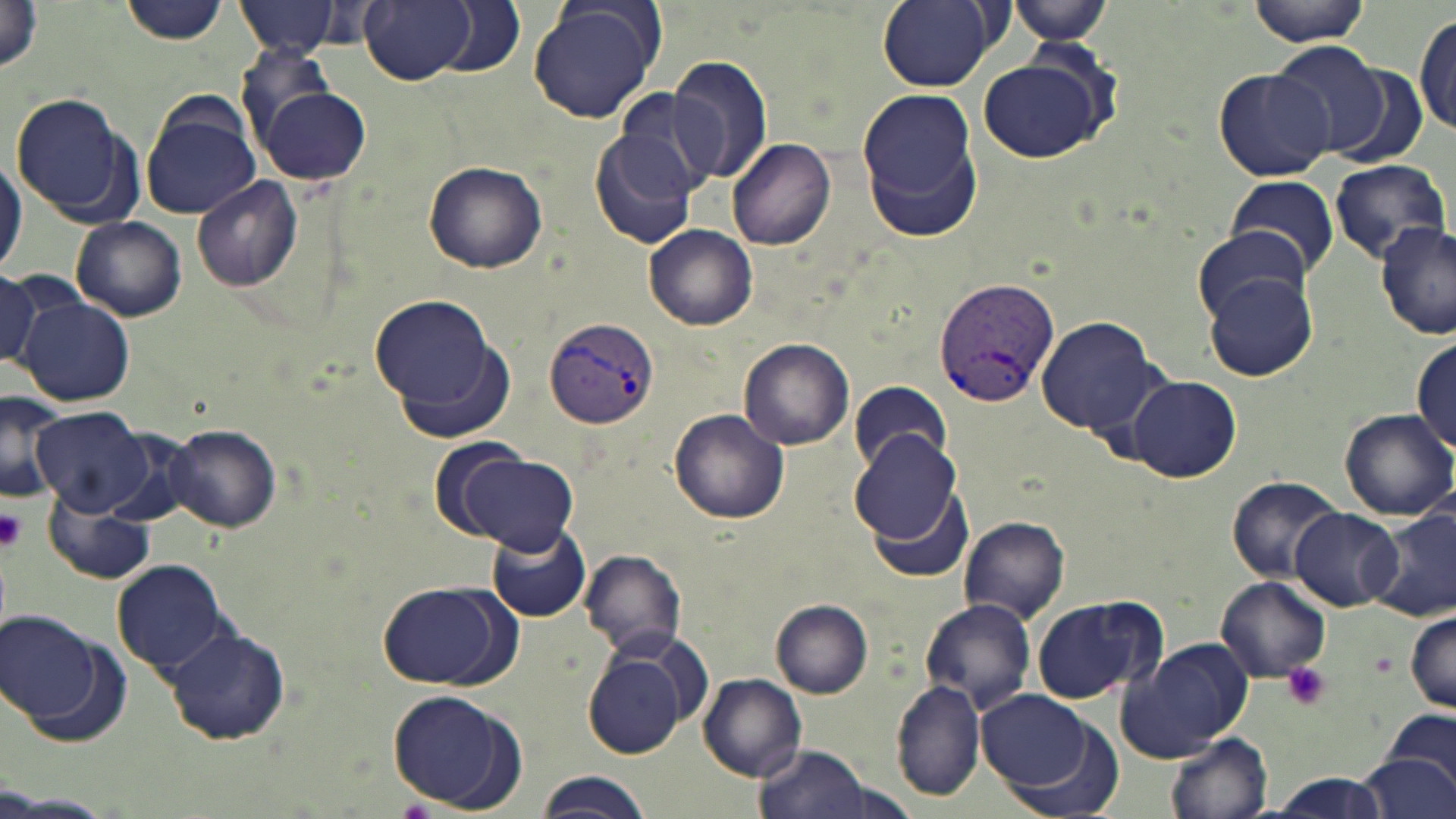
slide-level diagnosis = Plasmodium vivax
image size = 1456×819 pixels
modality = light microscopy
platelet locations = approximate bounding boxes as named x1/y1/x2/y2 corners in pixels: (x1=0, y1=507, x2=26, y2=552), (x1=1281, y1=663, x2=1331, y2=710)
magnification = 1000x
Plasmodium vivax-infected red blood cell locations = approximate bounding boxes as named x1/y1/x2/y2 corners in pixels: (x1=935, y1=280, x2=1058, y2=408), (x1=546, y1=317, x2=659, y2=428)
stain = May-Grünwald-Giemsa
uninfected red blood cell locations = approximate bounding boxes as named x1/y1/x2/y2 corners in pixels: (x1=1, y1=0, x2=44, y2=77), (x1=116, y1=0, x2=231, y2=44), (x1=235, y1=0, x2=348, y2=58), (x1=360, y1=0, x2=477, y2=85), (x1=877, y1=0, x2=998, y2=90), (x1=1008, y1=0, x2=1115, y2=46), (x1=1246, y1=0, x2=1374, y2=47), (x1=434, y1=1, x2=524, y2=77), (x1=528, y1=1, x2=664, y2=124), (x1=1414, y1=10, x2=1455, y2=141), (x1=1269, y1=42, x2=1393, y2=157), (x1=667, y1=55, x2=774, y2=188), (x1=977, y1=55, x2=1110, y2=162), (x1=1213, y1=67, x2=1335, y2=181), (x1=254, y1=81, x2=370, y2=186), (x1=857, y1=85, x2=979, y2=223), (x1=610, y1=90, x2=721, y2=199), (x1=7, y1=92, x2=141, y2=223), (x1=138, y1=99, x2=260, y2=219), (x1=169, y1=121, x2=293, y2=270), (x1=589, y1=124, x2=702, y2=250), (x1=728, y1=138, x2=836, y2=250), (x1=0, y1=150, x2=25, y2=279), (x1=1327, y1=158, x2=1450, y2=263), (x1=423, y1=159, x2=547, y2=272), (x1=1226, y1=175, x2=1341, y2=280), (x1=191, y1=177, x2=303, y2=292), (x1=72, y1=217, x2=186, y2=322), (x1=1375, y1=221, x2=1456, y2=340), (x1=643, y1=223, x2=756, y2=329), (x1=1188, y1=227, x2=1312, y2=326), (x1=0, y1=267, x2=66, y2=373), (x1=1206, y1=275, x2=1319, y2=380), (x1=371, y1=294, x2=499, y2=410), (x1=17, y1=296, x2=135, y2=407), (x1=1037, y1=316, x2=1158, y2=436), (x1=392, y1=328, x2=520, y2=445), (x1=1410, y1=337, x2=1456, y2=454), (x1=738, y1=338, x2=854, y2=451), (x1=1128, y1=374, x2=1242, y2=483), (x1=848, y1=381, x2=953, y2=475), (x1=0, y1=391, x2=66, y2=501), (x1=30, y1=405, x2=152, y2=517), (x1=669, y1=408, x2=792, y2=525), (x1=1339, y1=408, x2=1455, y2=521), (x1=166, y1=424, x2=281, y2=532), (x1=850, y1=430, x2=964, y2=547), (x1=455, y1=450, x2=577, y2=553), (x1=1225, y1=475, x2=1343, y2=581), (x1=865, y1=479, x2=976, y2=583), (x1=43, y1=493, x2=151, y2=584), (x1=1288, y1=507, x2=1404, y2=611), (x1=1369, y1=507, x2=1456, y2=622), (x1=958, y1=515, x2=1071, y2=625), (x1=486, y1=523, x2=591, y2=622), (x1=579, y1=548, x2=687, y2=656), (x1=112, y1=559, x2=229, y2=677), (x1=1215, y1=575, x2=1329, y2=682), (x1=376, y1=580, x2=516, y2=691), (x1=1028, y1=593, x2=1164, y2=705), (x1=918, y1=598, x2=1035, y2=715), (x1=771, y1=599, x2=873, y2=698), (x1=1406, y1=608, x2=1456, y2=712), (x1=2, y1=610, x2=102, y2=726), (x1=165, y1=624, x2=290, y2=745), (x1=1116, y1=638, x2=1255, y2=764), (x1=582, y1=641, x2=698, y2=759), (x1=699, y1=672, x2=809, y2=781), (x1=892, y1=678, x2=986, y2=804), (x1=387, y1=688, x2=524, y2=814), (x1=976, y1=691, x2=1097, y2=791), (x1=1375, y1=710, x2=1456, y2=789), (x1=1003, y1=717, x2=1125, y2=819), (x1=1167, y1=732, x2=1272, y2=818), (x1=753, y1=743, x2=877, y2=819), (x1=1360, y1=753, x2=1454, y2=819), (x1=535, y1=770, x2=652, y2=819), (x1=1254, y1=774, x2=1397, y2=817)
preparation = thin blood smear
field of view = single